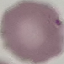

{
  "result": "negative for malaria parasites",
  "preparation": "thin smear",
  "stain": "Giemsa",
  "capture": "smartphone through the microscope eyepiece",
  "image_type": "automatically extracted cell patch, resized to 64 × 64 pixels"
}